Give the extent of all Plasmodium falciparum-infected red blood cells.
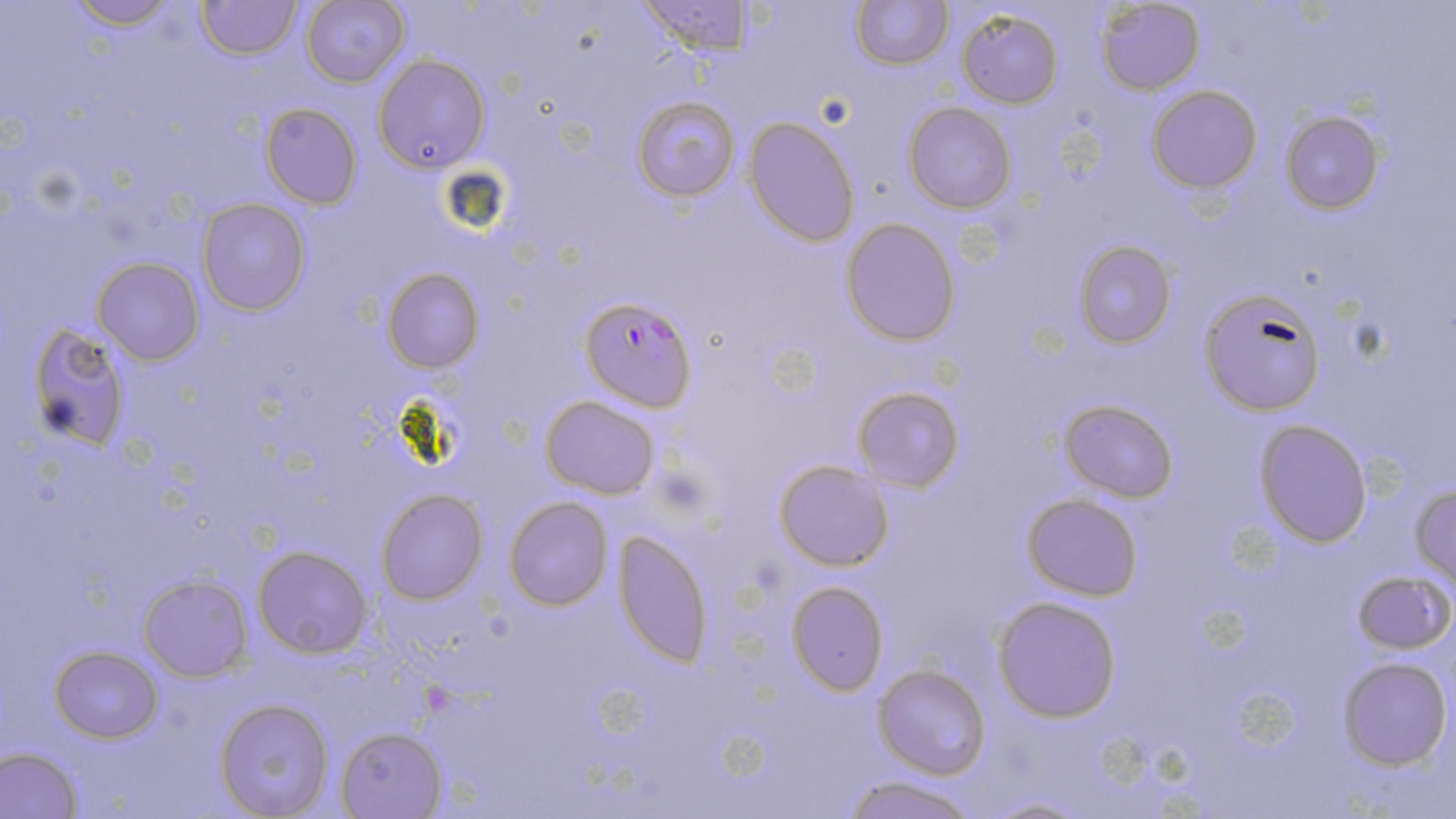
Approximate bounding boxes as (x1,y1)-(x2,y2) corner pairs in pixels.
Plasmodium falciparum-infected red blood cells: (582,292)-(694,410).

slide-level diagnosis = Plasmodium falciparum
magnification = 1000x
stain = May-Grünwald-Giemsa
uninfected red blood cell locations = approximate bounding boxes as (x1,y1)-(x2,y2) corner pairs in pixels: (66,0)-(180,28), (197,0)-(299,58), (636,0)-(752,55), (851,0)-(952,69), (1096,0)-(1205,93), (301,1)-(410,87), (956,7)-(1064,108), (373,53)-(492,173), (1146,85)-(1262,193), (630,94)-(740,202), (904,102)-(1016,213), (260,103)-(362,207), (1279,110)-(1386,217), (744,115)-(859,246), (198,199)-(310,317), (839,219)-(962,347), (1071,240)-(1175,349), (93,257)-(203,364), (380,268)-(484,374), (1201,289)-(1325,416), (25,322)-(134,451), (852,386)-(964,493), (540,394)-(660,498), (1059,398)-(1180,503), (1253,418)-(1375,547), (772,457)-(895,572), (1411,478)-(1456,592), (374,489)-(488,605), (1021,493)-(1143,603), (503,496)-(612,612), (614,528)-(713,666), (253,545)-(373,658), (1352,570)-(1454,657), (137,574)-(252,680), (784,580)-(890,694), (991,595)-(1124,721), (49,646)-(162,742), (1338,656)-(1452,770), (873,665)-(989,779), (215,698)-(335,818), (335,726)-(447,818), (1,746)-(82,819), (836,776)-(986,819)
field of view = single
modality = optical microscopy
preparation = thin blood smear
image size = 1456×819 pixels